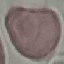
Summary:
  - Result: no malaria parasites detected
  - Preparation: thin smear
  - Capture: smartphone camera at the microscope eyepiece
  - Image type: automatically extracted cell patch, resized to 64 × 64 pixels
  - Stain: Giemsa